Locate every blood parasite and identify its species.
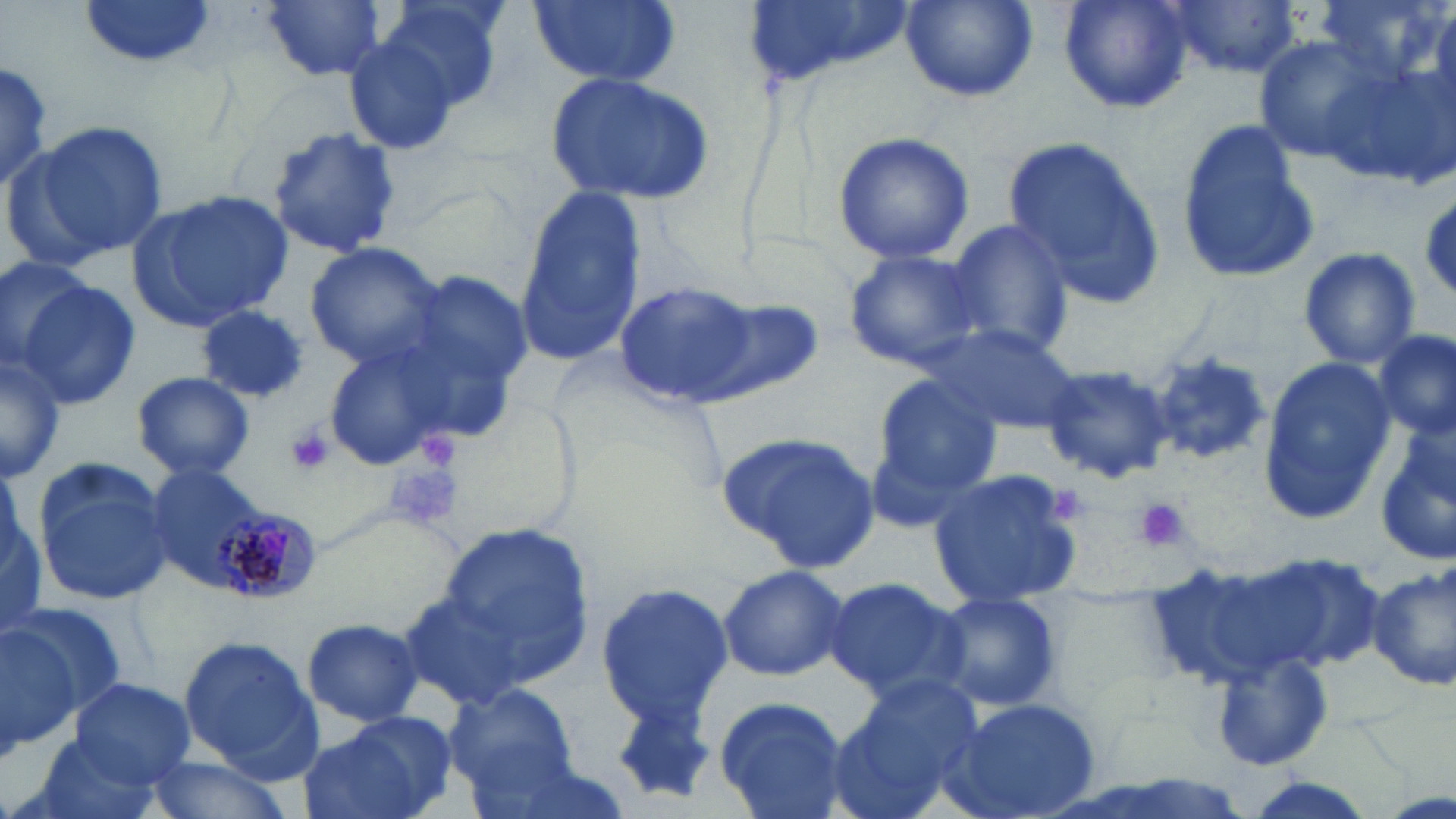

Approximate bounding boxes as [x1, y1, x2, y2] in pixels.
Plasmodium malariae-infected red blood cells: [207, 508, 328, 602].
No Plasmodium falciparum, Plasmodium ovale, Plasmodium vivax, Babesia divergens, or Trypanosoma brucei observed.

Uninfected red blood cell locations: [79, 0, 220, 70], [261, 0, 387, 82], [375, 0, 511, 110], [527, 0, 683, 88], [739, 0, 912, 94], [901, 0, 1036, 103], [1059, 0, 1195, 113], [1168, 0, 1305, 77], [1316, 0, 1439, 81], [340, 32, 464, 157], [1252, 33, 1403, 169], [0, 62, 57, 197], [547, 74, 716, 206], [16, 120, 167, 266], [1173, 120, 1319, 286], [265, 127, 401, 258], [831, 131, 975, 265], [1005, 137, 1168, 307], [512, 183, 648, 364], [127, 190, 296, 331], [1419, 197, 1456, 297], [946, 217, 1071, 357], [302, 241, 448, 370], [1297, 247, 1420, 368], [842, 248, 992, 371], [0, 255, 93, 367], [395, 271, 535, 409], [12, 275, 141, 412], [611, 277, 766, 406], [693, 297, 824, 403], [196, 305, 309, 405], [927, 325, 1080, 436], [1372, 332, 1455, 440], [318, 340, 467, 473], [0, 347, 64, 487], [1149, 351, 1273, 466], [1146, 352, 1275, 467], [1257, 357, 1394, 523], [1040, 364, 1176, 486], [131, 371, 256, 482], [873, 374, 1004, 499], [717, 430, 881, 575], [1372, 431, 1456, 566], [31, 458, 173, 606], [142, 461, 297, 601], [927, 469, 1088, 607], [433, 520, 595, 687], [1243, 551, 1387, 676], [717, 563, 849, 682], [1134, 563, 1318, 693], [1367, 563, 1456, 691], [823, 576, 971, 704], [592, 583, 733, 730], [398, 588, 534, 713], [936, 592, 1065, 713], [0, 609, 95, 756], [299, 618, 425, 727], [177, 632, 327, 780], [1212, 650, 1335, 770], [68, 677, 196, 787], [830, 679, 981, 816], [440, 685, 581, 801], [607, 687, 723, 805], [713, 694, 850, 819], [937, 697, 1102, 819], [299, 712, 456, 819], [26, 732, 171, 819], [141, 753, 300, 819], [1237, 777, 1383, 819]. Platelet locations: [285, 425, 335, 475], [414, 426, 462, 475], [387, 463, 462, 531], [1043, 483, 1090, 528], [1135, 498, 1188, 553]. Slide-level diagnosis: Plasmodium malariae. Optical microscopy. Image is 1456×819 pixels. May-Grünwald-Giemsa stain. 1000x magnification. Thin blood film. One field of a larger specimen.